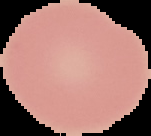

malaria status = uninfected
image type = cell region segmented out of the field of view; surrounding area masked to black
preparation = thin blood smear
image size = 151×136 pixels